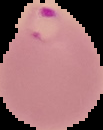

Summary:
  - Image size: 103×130 pixels
  - Preparation: thin blood film
  - Malaria status: parasitized
  - Image type: cell region segmented out of the field of view; surrounding area masked to black